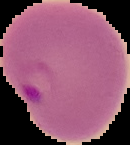
Segmented cell region on a black background. Result: Plasmodium parasites identified. From a thin blood smear. Image is 130×145 pixels.